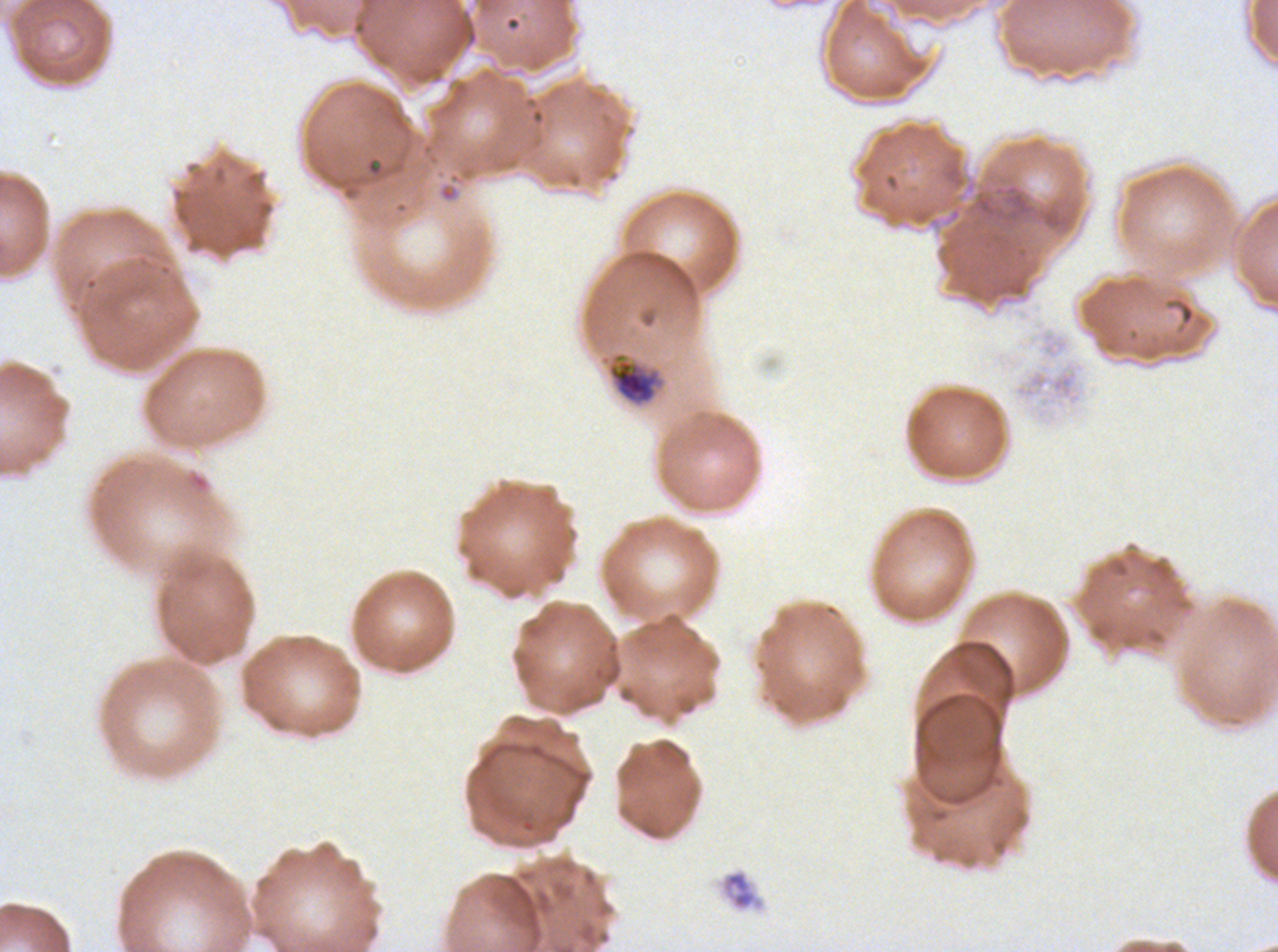
notation = approximate bounding rectangles given as corner coordinates in pixels from the top-left
debris locations = (x1=364, y1=156, x2=384, y2=178), (x1=720, y1=869, x2=764, y2=911)
mid trophozoite locations = (x1=606, y1=351, x2=666, y2=407)
stain = Giemsa
specimen = ex-vivo Plasmodium falciparum culture from a patient in The Gambia, grown for 24 to 48 hours
image size = 1278×952 pixels
field of view = sub-image separated from a larger composite
preparation = thin blood smear